Outline each uninfected red blood cell.
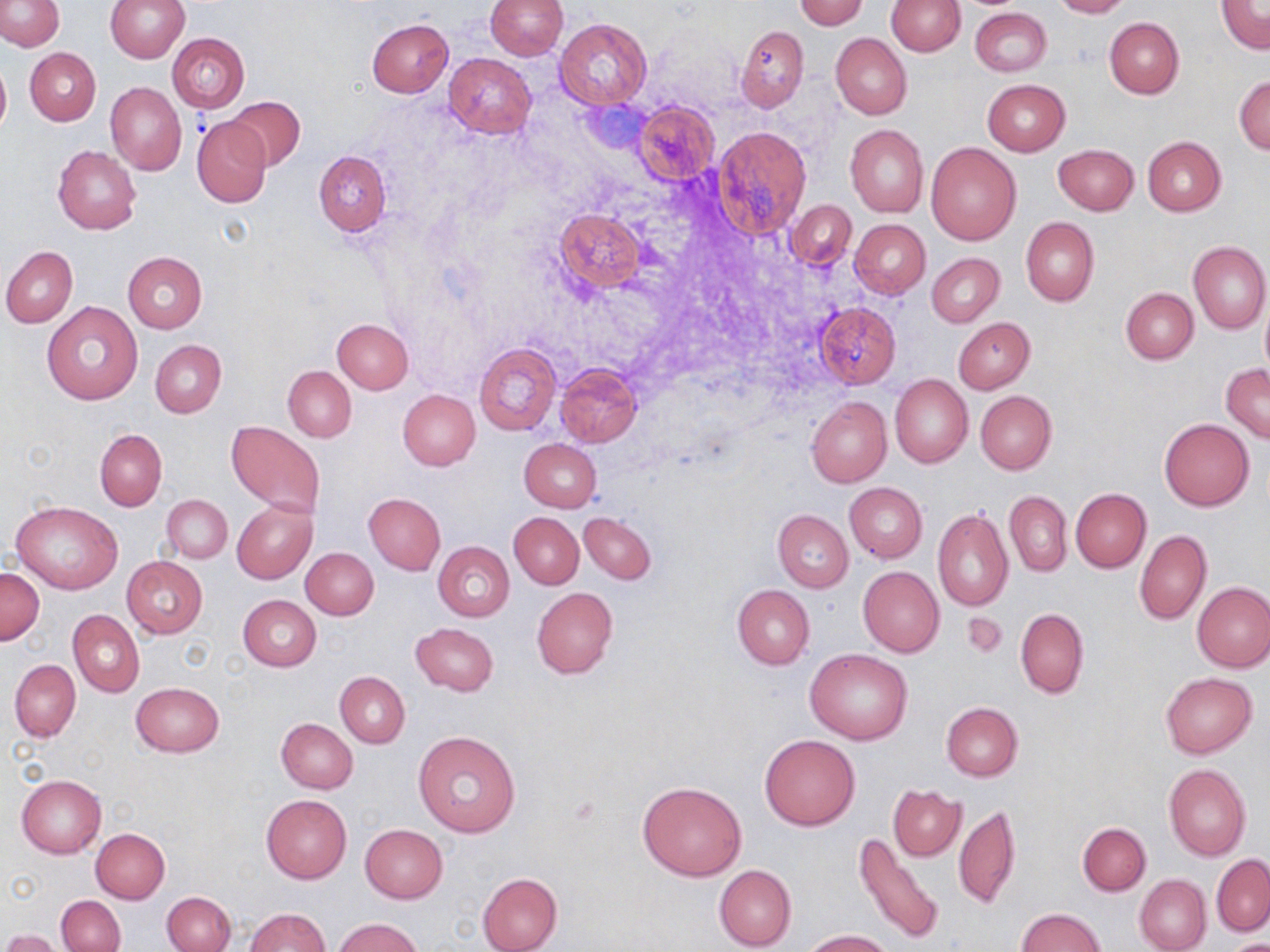
Approximate bounding boxes as (x1,y1)-(x2,y2) corner pairs in pixels.
Uninfected red blood cells: (0,0)-(65,50), (104,0)-(189,63), (485,0)-(568,60), (1048,0)-(1131,18), (1217,0)-(1269,53), (794,1)-(870,29), (888,1)-(965,55), (970,7)-(1051,76), (556,18)-(650,109), (1104,18)-(1183,98), (366,19)-(453,97), (735,25)-(809,112), (830,32)-(912,120), (167,33)-(250,113), (25,48)-(101,125), (443,53)-(537,137), (0,61)-(10,135), (1234,75)-(1270,155), (983,79)-(1070,155), (106,82)-(186,176), (227,98)-(306,170), (635,102)-(720,186), (192,117)-(271,207), (711,124)-(811,240), (845,124)-(928,217), (1143,137)-(1226,216), (926,142)-(1021,246), (1053,145)-(1139,215), (53,146)-(141,233), (314,151)-(390,236), (787,200)-(857,270), (554,208)-(646,293), (1020,217)-(1099,305), (850,219)-(931,297), (1188,241)-(1270,335), (1,246)-(77,327), (122,250)-(207,334), (926,252)-(1004,327), (1120,287)-(1198,364), (41,301)-(142,406), (1261,301)-(1270,377), (814,302)-(901,387), (331,317)-(414,394), (954,317)-(1035,393), (150,340)-(226,417), (474,342)-(561,434), (556,363)-(641,447), (1221,364)-(1270,443), (283,366)-(356,442), (890,373)-(972,468), (398,390)-(480,471), (975,391)-(1056,474), (806,395)-(891,488), (1160,419)-(1254,511), (227,420)-(325,518), (94,429)-(167,510), (518,438)-(601,511), (844,482)-(927,563), (1070,489)-(1150,572), (1004,491)-(1071,576), (161,494)-(232,564), (364,494)-(445,574), (12,500)-(123,595), (232,500)-(318,583), (932,507)-(1014,612), (773,510)-(854,592), (509,513)-(583,588), (579,513)-(657,584), (1134,528)-(1211,626), (433,541)-(514,622), (301,547)-(379,620), (121,555)-(208,638), (0,567)-(44,644), (858,567)-(944,657), (1192,582)-(1270,672), (732,584)-(814,669), (531,587)-(618,678), (238,595)-(321,670), (1016,608)-(1087,698), (69,610)-(144,696), (410,623)-(498,695), (806,648)-(913,745), (9,659)-(81,742), (335,671)-(410,747), (1161,672)-(1256,757), (130,682)-(223,757), (941,702)-(1022,782), (276,718)-(358,793), (413,731)-(522,838), (759,734)-(860,830), (1164,763)-(1251,861), (16,775)-(106,858), (638,779)-(748,881), (888,785)-(965,860), (261,793)-(351,882), (954,804)-(1021,909), (1078,822)-(1150,895), (359,823)-(449,904), (91,828)-(170,904), (854,833)-(945,945), (1212,854)-(1270,936), (714,864)-(797,951), (478,873)-(562,952), (1134,874)-(1210,952), (162,891)-(235,952), (56,895)-(125,952), (245,908)-(328,952), (1015,908)-(1106,951), (336,918)-(423,952), (3,929)-(60,952), (803,929)-(894,951), (1221,940)-(1270,952).

Slide-level diagnosis: no evidence of blood parasites. May-Grünwald-Giemsa stain. Optical microscopy. Image is 1270×952 pixels. Thin blood smear. Single field of view. 1000x magnification.